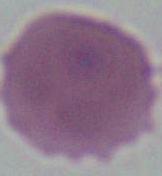

identification = erythrocyte
modality = micrograph
magnification = 1000x